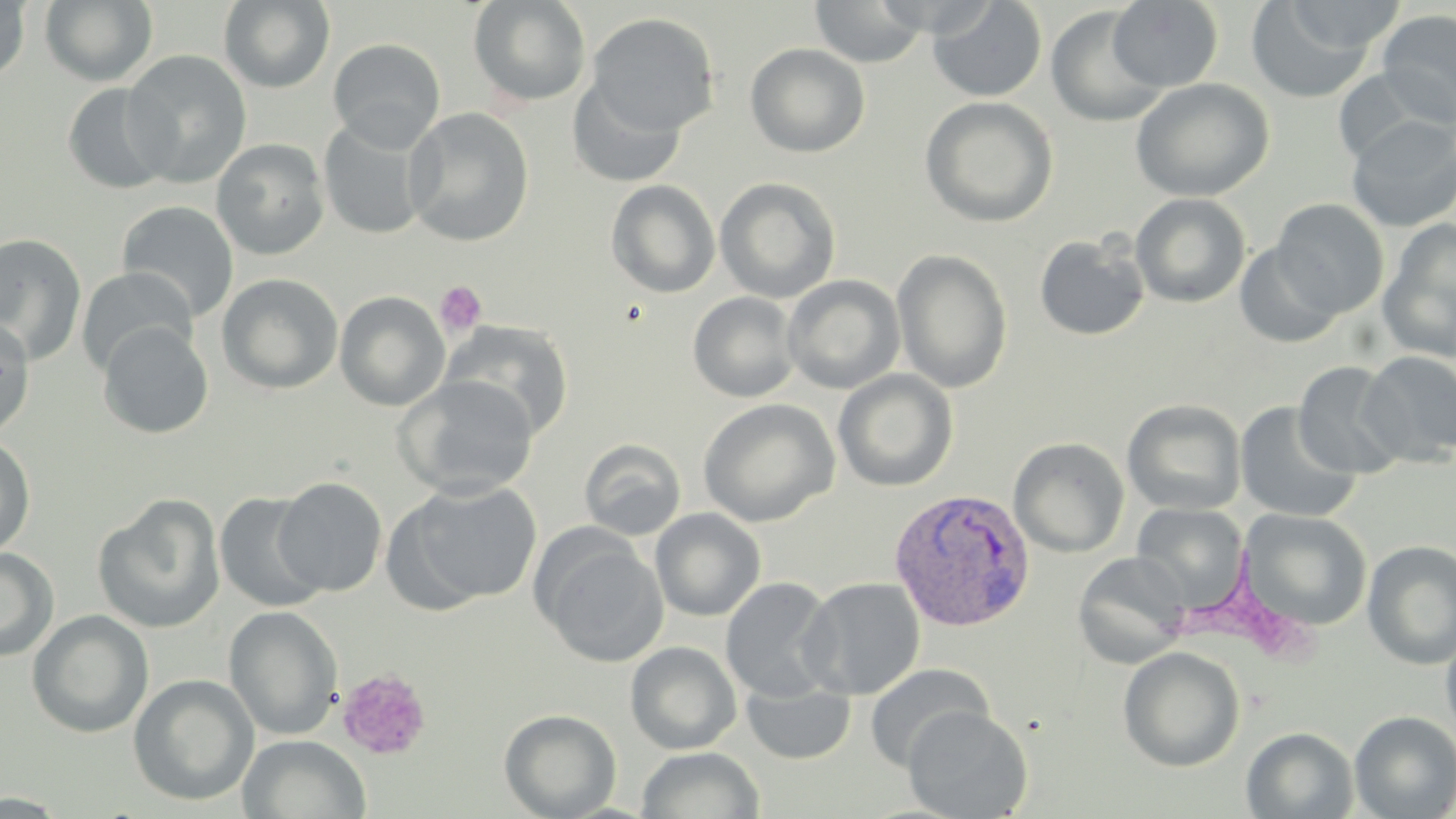
slide-level diagnosis = Plasmodium vivax
field of view = one of a larger specimen
modality = light microscopy
preparation = thin blood film
Plasmodium vivax-infected red blood cell locations = approximate bounding boxes as (x1,y1)-(x2,y2) corner pairs in pixels: (889,489)-(1036,632)
platelet locations = approximate bounding boxes as (x1,y1)-(x2,y2) corner pairs in pixels: (435,280)-(487,336), (336,669)-(431,760)
uninfected red blood cell locations = approximate bounding boxes as (x1,y1)-(x2,y2) corner pairs in pixels: (0,0)-(31,83), (468,0)-(592,108), (1280,0)-(1407,57), (39,1)-(158,87), (218,1)-(335,93), (811,1)-(928,68), (927,1)-(1048,103), (1107,1)-(1223,92), (1245,2)-(1378,104), (1045,6)-(1170,126), (1376,9)-(1456,127), (585,12)-(720,137), (327,38)-(446,150), (744,43)-(870,158), (122,50)-(252,187), (1330,68)-(1446,168), (568,76)-(688,189), (1130,78)-(1274,202), (61,82)-(175,194), (919,96)-(1059,227), (403,108)-(535,247), (318,115)-(433,241), (1345,115)-(1456,232), (211,138)-(330,261), (714,177)-(841,303), (606,180)-(721,298), (1130,192)-(1251,308), (1271,198)-(1389,319), (116,200)-(239,322), (1377,220)-(1456,363), (0,232)-(88,367), (1034,233)-(1150,341), (1234,241)-(1345,348), (892,248)-(1013,393), (76,266)-(197,377), (216,273)-(344,395), (782,275)-(906,395), (334,291)-(450,412), (687,291)-(803,403), (0,316)-(36,439), (440,319)-(574,441), (97,321)-(214,439), (1359,352)-(1456,466), (1293,361)-(1408,479), (833,369)-(958,491), (394,376)-(539,500), (698,397)-(839,527), (1122,399)-(1247,516), (1234,402)-(1361,523), (0,435)-(36,557), (1008,437)-(1130,558), (579,438)-(687,541), (273,476)-(388,596), (394,480)-(545,609), (214,491)-(328,613), (92,494)-(226,635), (1132,503)-(1249,608), (650,508)-(766,622), (1240,508)-(1373,631), (536,535)-(668,668), (1361,540)-(1456,670), (0,547)-(59,661), (1072,551)-(1191,669), (720,576)-(839,702), (799,577)-(926,700), (223,604)-(343,740), (27,609)-(154,738), (1440,630)-(1456,744), (625,641)-(742,754), (1118,646)-(1245,772), (864,663)-(994,772), (128,673)-(259,806), (742,680)-(856,764), (902,705)-(1032,818), (499,708)-(622,819), (1349,710)-(1456,818), (1241,727)-(1359,818), (238,734)-(371,819), (636,747)-(765,819), (0,792)-(72,818)
stain = May-Grünwald-Giemsa
magnification = 1000x
image size = 1456×819 pixels